Assess this cell for malaria.
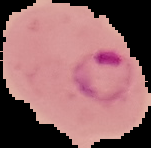
Parasitized.

From a thin blood smear. Image is 151×148 pixels. The area outside the segmented cell region is set to black.